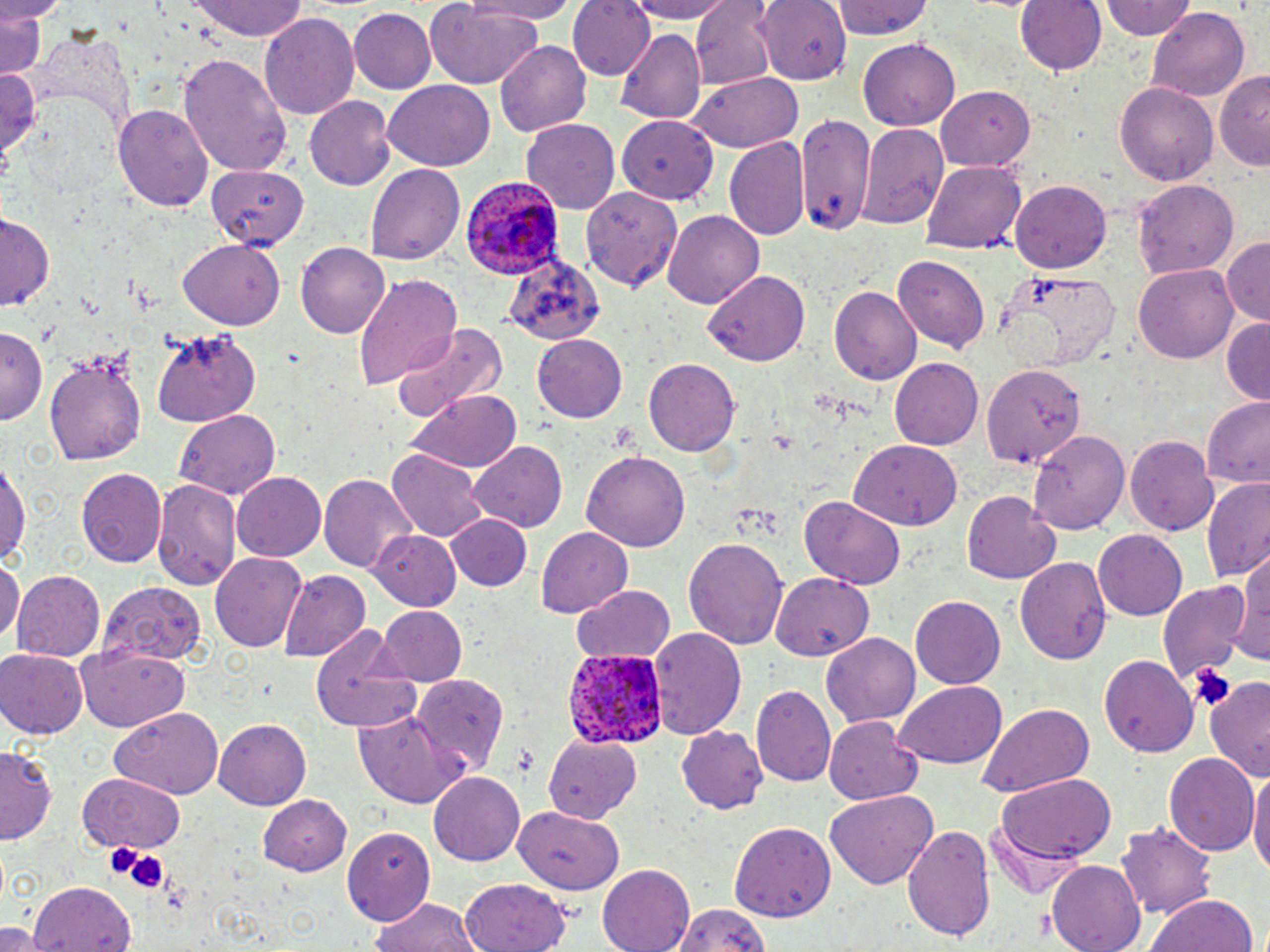

Summary:
  - Coordinate format: approximate bounding boxes as named x1/y1/x2/y2 corners in pixels
  - Plasmodium ovale-infected red blood cell locations: (x1=460, y1=177, x2=561, y2=280), (x1=564, y1=648, x2=667, y2=749)
  - Uninfected red blood cell locations: (x1=0, y1=0, x2=60, y2=25), (x1=186, y1=0, x2=312, y2=41), (x1=463, y1=0, x2=579, y2=23), (x1=568, y1=0, x2=655, y2=81), (x1=626, y1=0, x2=736, y2=23), (x1=830, y1=0, x2=936, y2=41), (x1=1014, y1=0, x2=1105, y2=77), (x1=1102, y1=0, x2=1197, y2=41), (x1=694, y1=1, x2=778, y2=87), (x1=754, y1=1, x2=850, y2=81), (x1=424, y1=3, x2=544, y2=90), (x1=1, y1=7, x2=46, y2=80), (x1=1148, y1=7, x2=1250, y2=101), (x1=348, y1=8, x2=434, y2=93), (x1=260, y1=11, x2=359, y2=119), (x1=23, y1=26, x2=132, y2=134), (x1=614, y1=28, x2=706, y2=125), (x1=496, y1=40, x2=590, y2=136), (x1=858, y1=40, x2=962, y2=130), (x1=181, y1=52, x2=290, y2=176), (x1=0, y1=63, x2=49, y2=171), (x1=1217, y1=71, x2=1270, y2=173), (x1=689, y1=75, x2=802, y2=152), (x1=383, y1=81, x2=495, y2=171), (x1=1116, y1=82, x2=1218, y2=187), (x1=936, y1=84, x2=1037, y2=170), (x1=305, y1=98, x2=395, y2=190), (x1=112, y1=101, x2=214, y2=215), (x1=792, y1=114, x2=877, y2=234), (x1=617, y1=116, x2=718, y2=205), (x1=521, y1=118, x2=623, y2=211), (x1=859, y1=123, x2=948, y2=228), (x1=724, y1=136, x2=811, y2=242), (x1=201, y1=160, x2=311, y2=254), (x1=921, y1=162, x2=1025, y2=254), (x1=366, y1=163, x2=464, y2=264), (x1=1012, y1=179, x2=1112, y2=271), (x1=1134, y1=180, x2=1239, y2=276), (x1=585, y1=187, x2=685, y2=295), (x1=662, y1=210, x2=764, y2=306), (x1=0, y1=214, x2=53, y2=308), (x1=1221, y1=237, x2=1269, y2=327), (x1=178, y1=239, x2=283, y2=331), (x1=296, y1=241, x2=390, y2=338), (x1=501, y1=250, x2=605, y2=344), (x1=893, y1=257, x2=991, y2=354), (x1=1134, y1=264, x2=1239, y2=366), (x1=704, y1=271, x2=810, y2=366), (x1=353, y1=274, x2=464, y2=391), (x1=829, y1=287, x2=922, y2=385), (x1=1221, y1=318, x2=1269, y2=404), (x1=392, y1=322, x2=506, y2=424), (x1=153, y1=329, x2=264, y2=428), (x1=0, y1=331, x2=45, y2=427), (x1=532, y1=333, x2=628, y2=423), (x1=44, y1=348, x2=150, y2=468), (x1=891, y1=357, x2=986, y2=450), (x1=644, y1=358, x2=740, y2=457), (x1=980, y1=359, x2=1090, y2=471), (x1=407, y1=390, x2=520, y2=474), (x1=1200, y1=398, x2=1270, y2=488), (x1=176, y1=412, x2=279, y2=500), (x1=1028, y1=428, x2=1129, y2=531), (x1=1126, y1=433, x2=1219, y2=535), (x1=850, y1=439, x2=964, y2=528), (x1=469, y1=442, x2=566, y2=533), (x1=385, y1=449, x2=487, y2=542), (x1=580, y1=451, x2=690, y2=552), (x1=0, y1=456, x2=30, y2=572), (x1=75, y1=468, x2=167, y2=571), (x1=231, y1=472, x2=326, y2=562), (x1=319, y1=473, x2=418, y2=573), (x1=153, y1=478, x2=243, y2=589), (x1=1200, y1=478, x2=1270, y2=581), (x1=960, y1=490, x2=1060, y2=584), (x1=801, y1=496, x2=907, y2=589), (x1=444, y1=514, x2=532, y2=593), (x1=537, y1=526, x2=635, y2=618), (x1=1093, y1=528, x2=1189, y2=619), (x1=371, y1=529, x2=461, y2=612), (x1=684, y1=536, x2=788, y2=651), (x1=210, y1=550, x2=308, y2=651), (x1=1235, y1=550, x2=1269, y2=671), (x1=0, y1=556, x2=22, y2=648), (x1=1017, y1=558, x2=1112, y2=665), (x1=280, y1=569, x2=368, y2=661), (x1=12, y1=571, x2=106, y2=664), (x1=771, y1=573, x2=875, y2=661), (x1=1157, y1=581, x2=1250, y2=684), (x1=97, y1=582, x2=206, y2=666), (x1=572, y1=584, x2=674, y2=665), (x1=911, y1=596, x2=1006, y2=690), (x1=375, y1=606, x2=467, y2=688), (x1=311, y1=626, x2=426, y2=732), (x1=650, y1=627, x2=746, y2=740), (x1=822, y1=634, x2=919, y2=727), (x1=76, y1=645, x2=191, y2=731), (x1=0, y1=649, x2=88, y2=739), (x1=1099, y1=656, x2=1197, y2=756), (x1=409, y1=675, x2=511, y2=773), (x1=1201, y1=676, x2=1270, y2=783), (x1=895, y1=682, x2=1008, y2=769), (x1=752, y1=684, x2=839, y2=787), (x1=977, y1=704, x2=1095, y2=797), (x1=112, y1=709, x2=224, y2=796), (x1=353, y1=709, x2=460, y2=808), (x1=825, y1=716, x2=927, y2=806), (x1=214, y1=717, x2=311, y2=808), (x1=677, y1=726, x2=767, y2=814), (x1=545, y1=736, x2=642, y2=823), (x1=1, y1=745, x2=60, y2=844), (x1=1166, y1=752, x2=1259, y2=858), (x1=1249, y1=767, x2=1270, y2=882), (x1=428, y1=770, x2=529, y2=865), (x1=77, y1=773, x2=187, y2=850), (x1=998, y1=774, x2=1117, y2=862), (x1=826, y1=792, x2=937, y2=887), (x1=257, y1=795, x2=352, y2=876), (x1=514, y1=808, x2=623, y2=895), (x1=1118, y1=821, x2=1215, y2=919), (x1=730, y1=823, x2=836, y2=920), (x1=903, y1=826, x2=994, y2=946), (x1=342, y1=827, x2=436, y2=925), (x1=1045, y1=862, x2=1147, y2=952), (x1=598, y1=864, x2=695, y2=952), (x1=461, y1=877, x2=571, y2=951), (x1=27, y1=885, x2=137, y2=952), (x1=1146, y1=891, x2=1257, y2=952), (x1=371, y1=897, x2=483, y2=952), (x1=670, y1=904, x2=774, y2=952), (x1=0, y1=923, x2=44, y2=952)
  - Platelet locations: (x1=1189, y1=662, x2=1237, y2=714), (x1=103, y1=842, x2=162, y2=891)
  - Slide-level diagnosis: Plasmodium ovale
  - Image size: 1270×952 pixels
  - Magnification: 1000x
  - Stain: May-Grünwald-Giemsa
  - Preparation: thin blood smear
  - Modality: light microscopy
  - Field of view: single